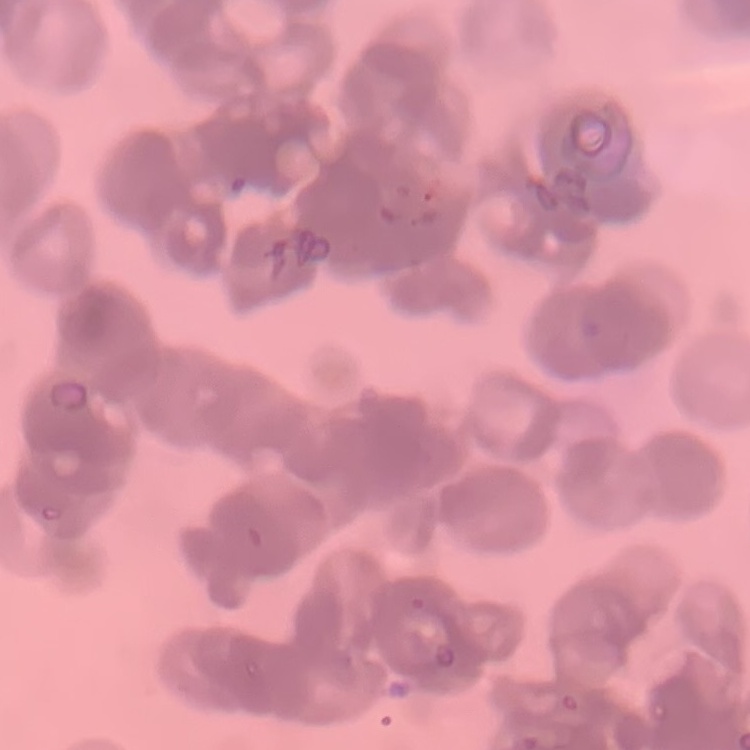

Summary:
  - Erythrocyte morphology: rouleaux formation
  - Preparation: thin blood film
  - Image type: square crop of a larger photomicrograph
  - Stain: Field's or Giemsa